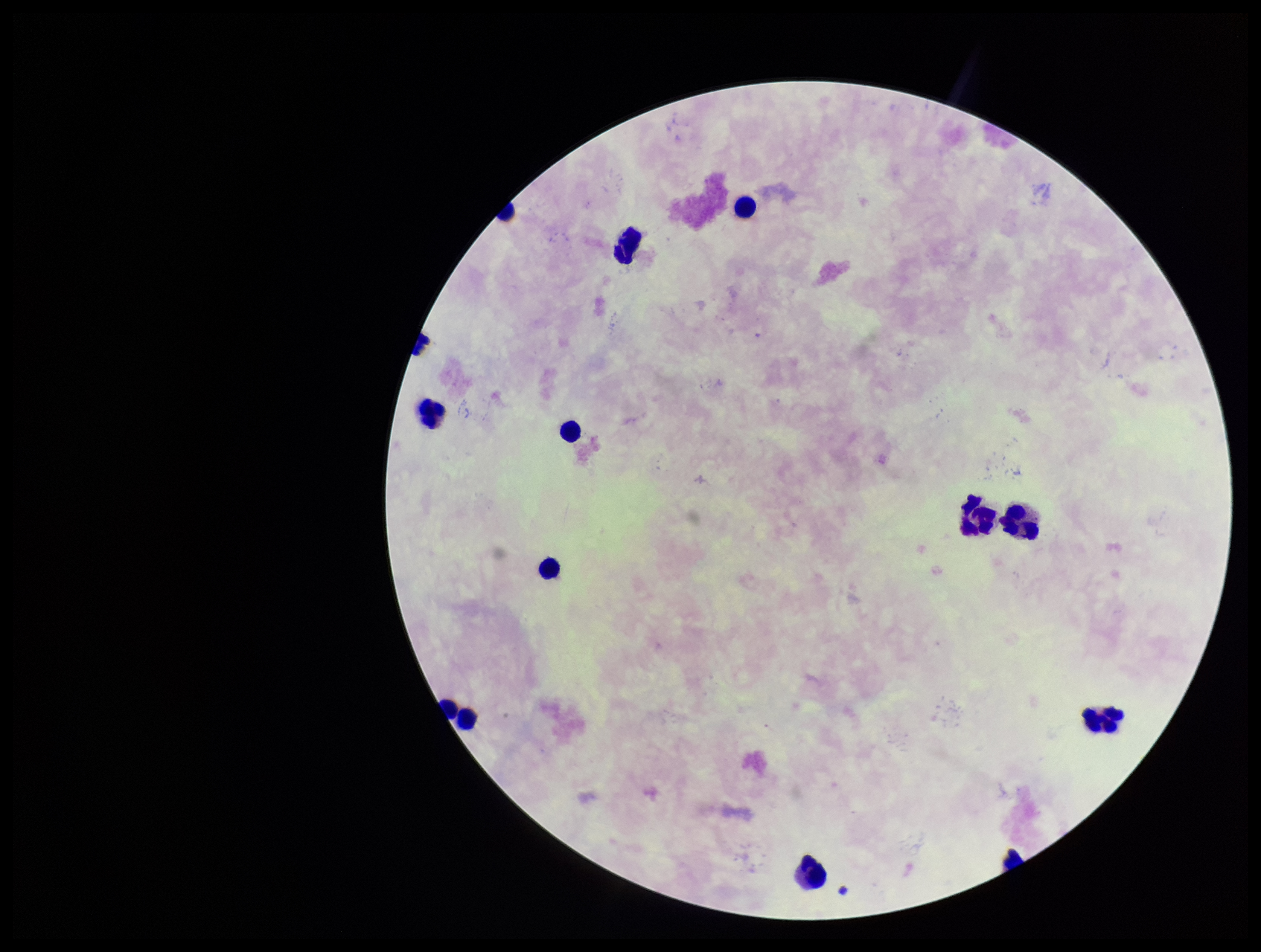

field_of_view: one from this slide
stain: Giemsa
patient_malaria_status: negative
plasmodium_parasites: none seen
parasite_count: 0
leukocyte_count: 12
image_size: 1261×952 pixels
preparation: thick
capture: smartphone photograph through the microscope eyepiece